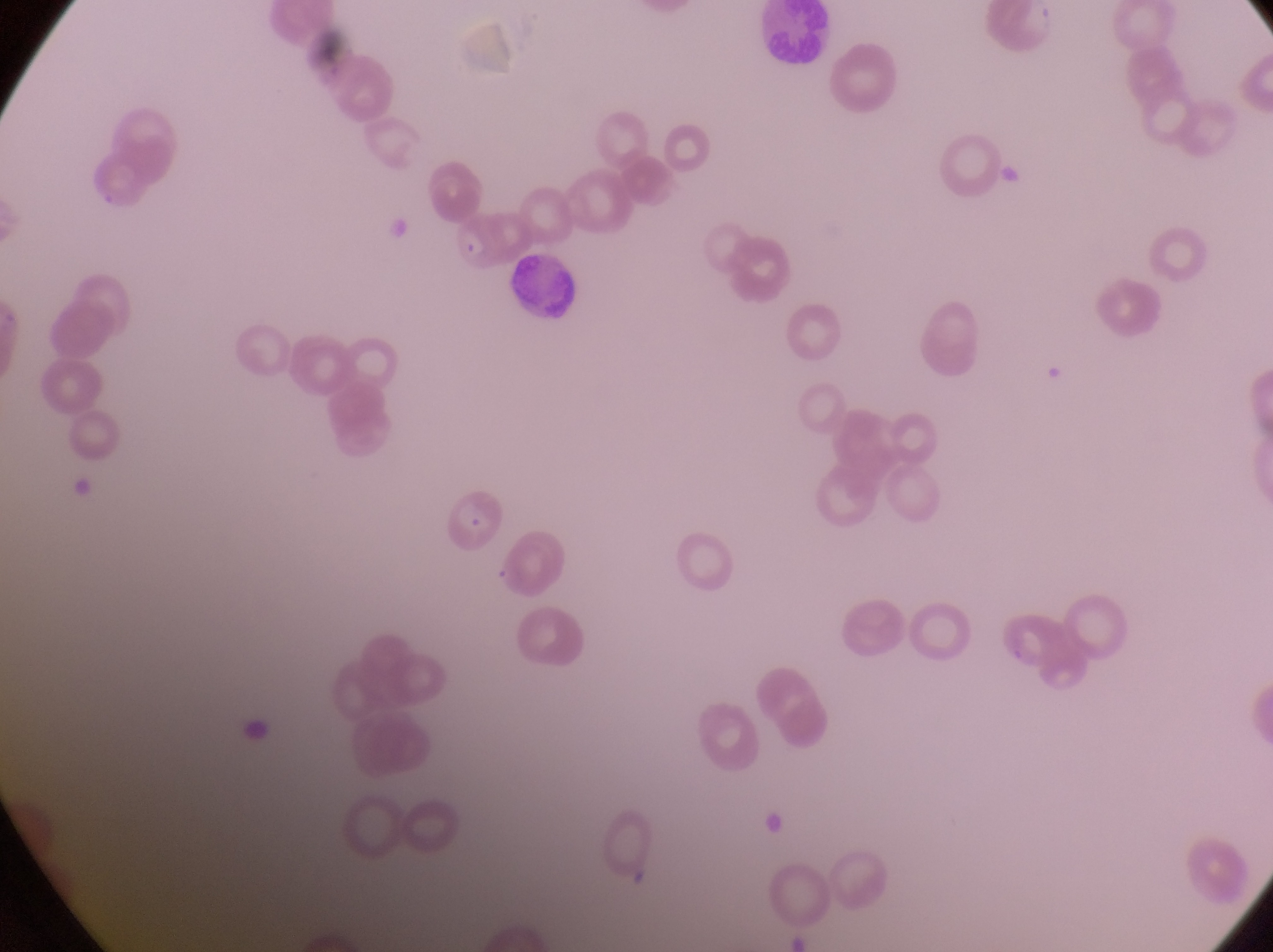
image size = 1273×952 pixels
country = Uganda
preparation = thin blood smear
parasitised red blood cell locations = approximate bounding boxes as [left, top, right, bottom] in pixels: [445, 210, 500, 278], [438, 486, 505, 556]
field of view = single
capture = smartphone photograph through the eyepiece of an Olympus CX-23 microscope
magnification = 1000x
leukocyte locations = approximate bounding boxes as [left, top, right, bottom] in pixels: [762, 3, 833, 70], [512, 254, 583, 320]